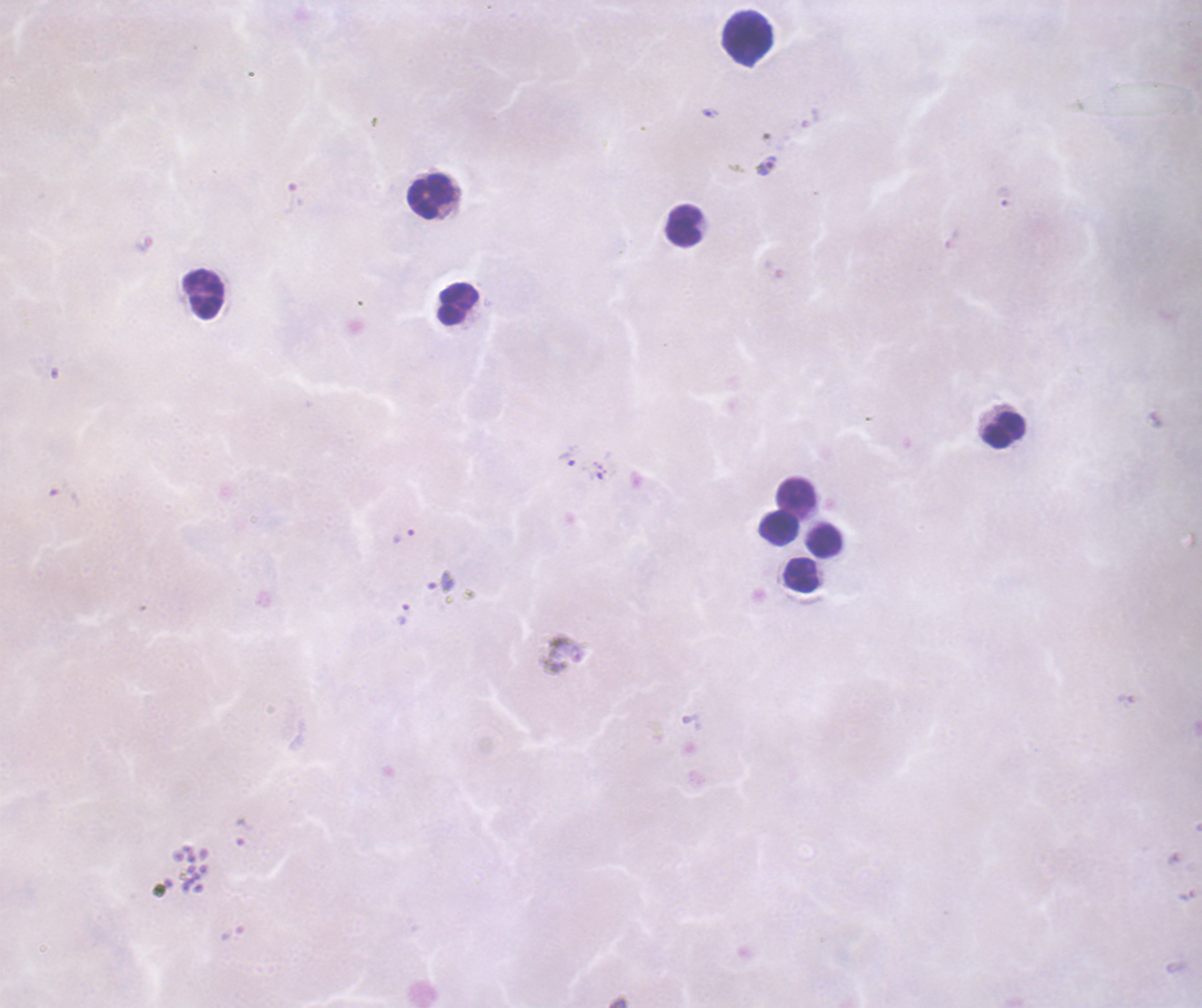
Approximate centers as {x, y} in pixels. Leukocyte locations: {748, 38}, {431, 196}, {684, 226}, {203, 296}, {458, 304}, {1004, 430}, {796, 497}, {779, 529}, {825, 542}, {801, 575}. Trophozoite locations: {710, 113}, {766, 166}, {568, 456}, {403, 536}, {441, 581}, {402, 614}, {242, 832}. Previously used in a real diagnosis. Image is 1202×1008 pixels. Thick smear of blood. Single field of view. Background quality: unsatisfactory. Romanowsky-stained preparation. Captured at 100x magnification. Coloration quality: bad. Result: positive for malaria parasites.